Assess for malaria.
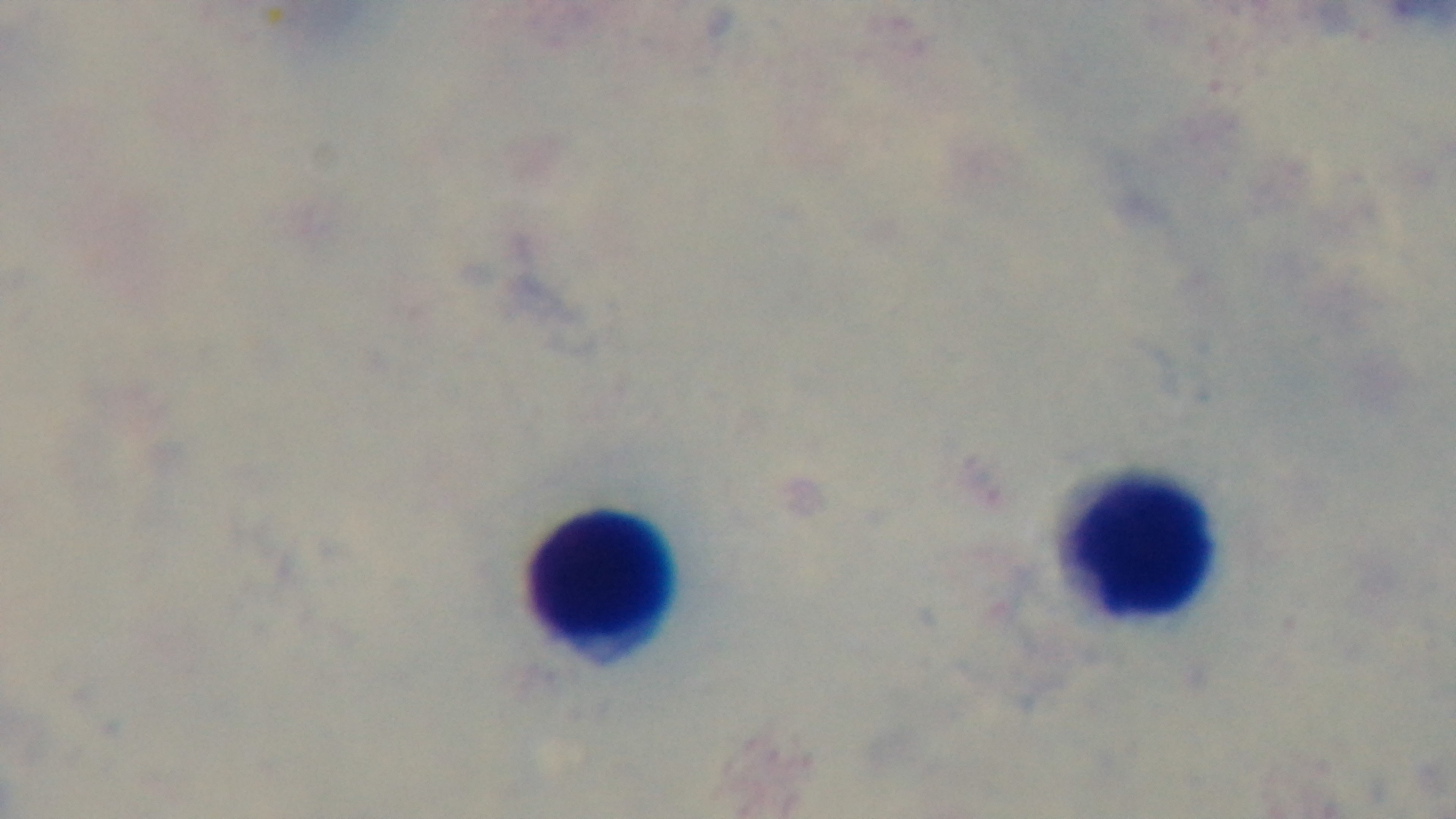

Uninfected.

Giemsa-stained. Preparation: thick blood film. Captured with a mounted 4K digital camera. Light microscopy. Oil-immersion objective, 100x. Single field of view.